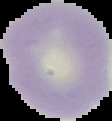
Summary:
  - Image size: 112×121 pixels
  - Image type: cell region segmented out of the field of view; surrounding area masked to black
  - Preparation: thin blood film
  - Malaria status: uninfected